Assess this cell for malaria.
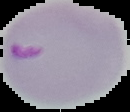

Parasitized.

Image is 130×112 pixels. Cell region segmented out of the field of view; the surrounding area is masked to black. From a thin blood film.